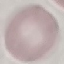

Summary:
  - Malaria status: uninfected
  - Preparation: thin smear
  - Stain: Giemsa
  - Image type: cell patch, automatically extracted from a larger field of view and resized to 64 × 64 pixels
  - Capture: smartphone through the microscope eyepiece